Locate every blood parasite and identify its species.
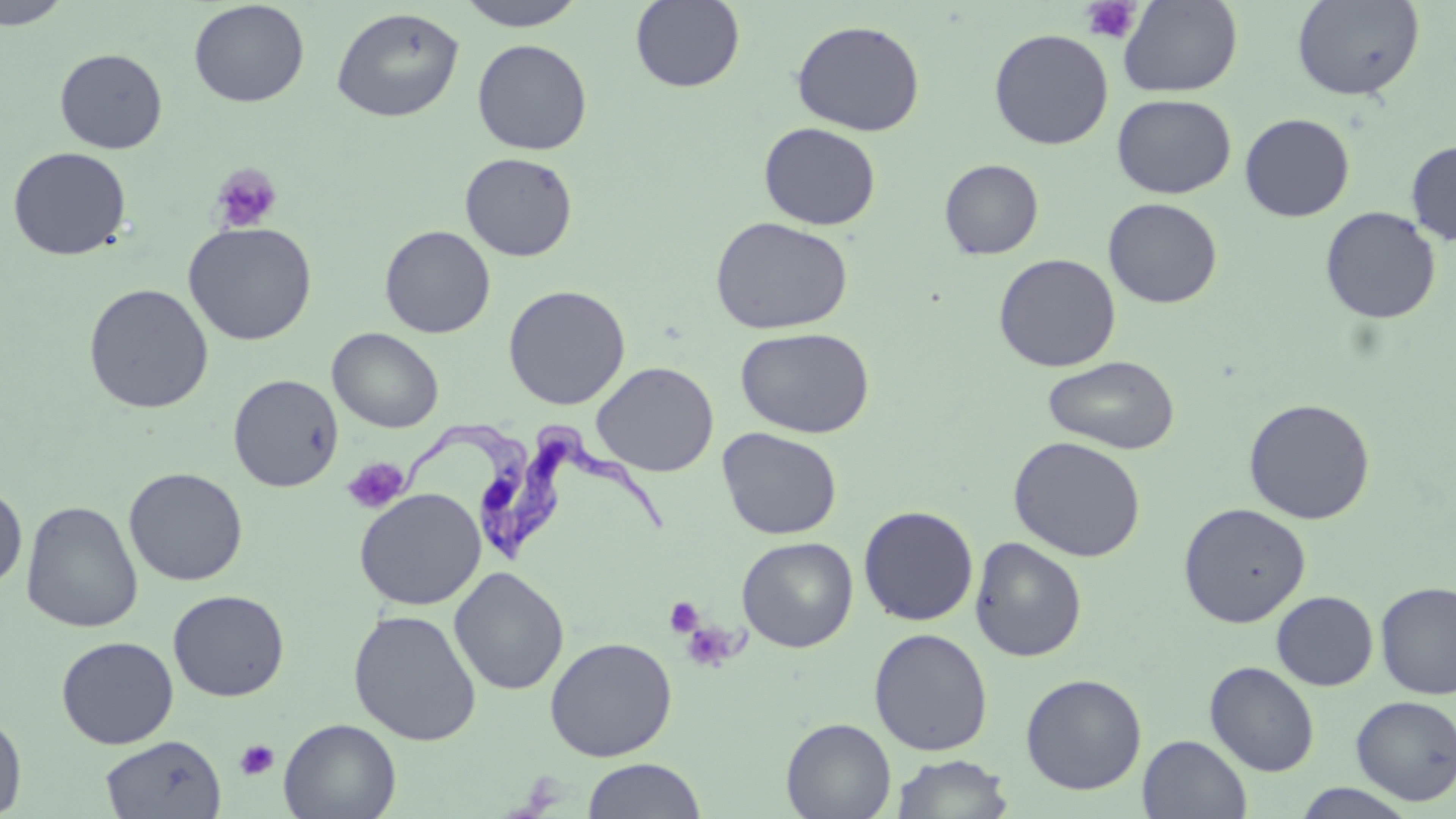

Approximate bounding boxes as [x1, y1, x2, y2] in pixels.
Trypanosoma brucei: [511, 416, 669, 562], [411, 422, 533, 562].
No Plasmodium falciparum, Plasmodium ovale, Plasmodium malariae, Plasmodium vivax, or Babesia divergens observed.

{
  "slide_level_diagnosis": "Trypanosoma brucei",
  "preparation": "thin blood film",
  "platelet_locations": "approximate bounding boxes as [x1, y1, x2, y2] in pixels: [1081, 1, 1142, 44], [210, 163, 283, 233], [341, 457, 410, 515], [664, 597, 705, 639], [680, 620, 741, 673], [234, 738, 280, 782]",
  "modality": "optical microscopy",
  "field_of_view": "one of a larger specimen",
  "stain": "May-Grünwald-Giemsa",
  "uninfected_red_blood_cell_locations": "approximate bounding boxes as [x1, y1, x2, y2] in pixels: [0, 0, 74, 30], [454, 0, 589, 31], [630, 0, 745, 92], [1118, 0, 1243, 97], [1292, 0, 1424, 101], [188, 1, 309, 107], [331, 7, 464, 122], [791, 19, 925, 136], [989, 28, 1114, 149], [472, 39, 592, 155], [55, 47, 167, 153], [1111, 93, 1236, 198], [1239, 113, 1354, 222], [758, 122, 881, 231], [1406, 140, 1456, 246], [7, 146, 132, 261], [459, 152, 578, 261], [939, 158, 1044, 259], [1103, 197, 1222, 308], [1320, 206, 1441, 324], [710, 216, 854, 335], [182, 222, 317, 345], [379, 225, 495, 337], [993, 253, 1121, 372], [83, 283, 214, 414], [503, 284, 631, 410], [327, 327, 444, 433], [735, 327, 875, 438], [1042, 354, 1181, 453], [591, 361, 718, 476], [228, 374, 343, 491], [1243, 398, 1376, 524], [718, 427, 842, 539], [1008, 435, 1146, 562], [124, 467, 248, 586], [0, 481, 28, 591], [354, 488, 486, 610], [21, 500, 142, 633], [1178, 502, 1311, 628], [858, 505, 979, 626], [737, 536, 858, 652], [970, 537, 1087, 662], [448, 566, 569, 696], [1375, 580, 1456, 700], [167, 590, 290, 701], [1271, 590, 1378, 691], [348, 609, 482, 746], [869, 627, 993, 756], [56, 635, 179, 749], [544, 636, 678, 761], [1205, 661, 1319, 776], [1020, 673, 1147, 795], [1351, 695, 1456, 805], [0, 713, 27, 817], [278, 717, 401, 819], [781, 718, 896, 819], [100, 734, 226, 818], [1139, 734, 1252, 819], [890, 754, 1015, 818], [580, 758, 707, 818], [1292, 784, 1420, 818]",
  "magnification": "1000x",
  "image_size": "1456×819 pixels"
}